Assess this cell for malaria.
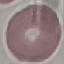

Uninfected.

stain = Giemsa
image type = automatically extracted cell patch, resized to 64 × 64 pixels
capture = smartphone camera at the microscope eyepiece
preparation = thin blood film